Which red blood cells are Plasmodium falciparum-infected, and which are of indeterminate infection status?
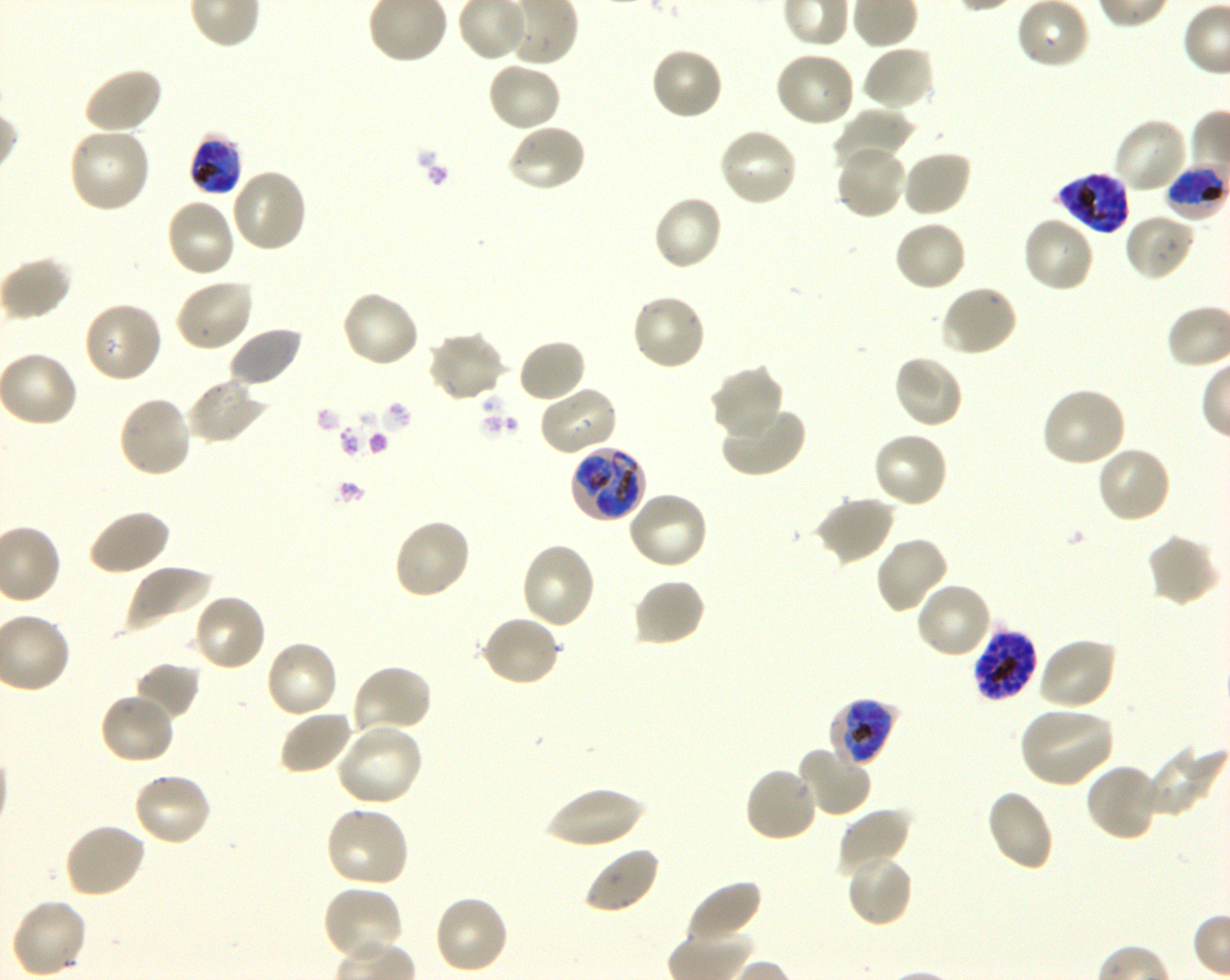

Approximate bounding boxes as (x1, y1, x2, y2) in pixels. Not every red blood cell is marked. A life-cycle stage — or a range of stages, where the recorded stages span more than one — follows each staged infected red blood cell.
Infected red blood cells: (188, 134, 243, 197) late trophozoite to late schizont; (1164, 165, 1226, 219) early trophozoite to early schizont; (1058, 171, 1131, 235) schizont; (569, 445, 648, 524) trophozoite; (972, 629, 1038, 701) schizont; (829, 697, 900, 768) early trophozoite to late schizont.
No red blood cells of indeterminate infection status observed.

locations of uninfected red blood cells = (1016, 0, 1090, 70), (649, 45, 725, 121), (860, 45, 935, 113), (775, 51, 857, 129), (486, 59, 564, 132), (81, 66, 163, 136), (830, 110, 912, 173), (1112, 117, 1189, 194), (505, 122, 587, 194), (68, 126, 152, 215), (717, 126, 799, 208), (835, 144, 907, 219), (901, 149, 972, 218), (230, 168, 309, 253), (652, 194, 725, 272), (165, 196, 237, 279), (1123, 212, 1197, 282), (1020, 214, 1096, 294), (893, 219, 967, 293), (173, 279, 255, 353), (938, 283, 1019, 357), (340, 289, 421, 369), (630, 293, 708, 372), (82, 301, 163, 384), (228, 326, 304, 389), (426, 329, 506, 404), (517, 338, 588, 404), (892, 353, 965, 431), (708, 364, 785, 440), (186, 377, 268, 445), (538, 384, 619, 457), (1039, 385, 1127, 468), (117, 394, 193, 478), (720, 405, 806, 478), (872, 430, 950, 510), (1095, 444, 1172, 525), (626, 490, 710, 571), (814, 494, 896, 566), (87, 508, 170, 577), (392, 517, 472, 600), (1146, 532, 1220, 608), (874, 535, 950, 615), (520, 541, 597, 630), (123, 563, 211, 635), (632, 578, 707, 648), (914, 582, 994, 661), (192, 592, 269, 672), (480, 614, 562, 689), (1036, 636, 1116, 711), (264, 640, 339, 720), (133, 661, 201, 722), (351, 664, 434, 737), (98, 692, 177, 766), (1017, 705, 1116, 788), (279, 710, 354, 776), (334, 723, 424, 808), (1144, 743, 1225, 818), (796, 744, 873, 818), (1085, 761, 1162, 843), (743, 765, 820, 844), (131, 770, 213, 847), (544, 787, 645, 849), (984, 788, 1054, 872), (324, 806, 411, 889), (836, 807, 912, 877), (63, 822, 146, 899), (583, 845, 661, 915), (844, 852, 913, 928), (686, 879, 762, 946), (322, 885, 405, 963), (432, 895, 510, 976), (10, 896, 88, 978)
life-cycle stages observed = trophozoite, schizont
image size = 1230×980 pixels
culture = Plasmodium falciparum strain 3D7, shaking, in vitro
donor blood group = O+
objective = 100x, oil immersion, numerical aperture 1.30
stain = Giemsa
field of view = one from this slide
preparation = thin blood smear